Outline platelets.
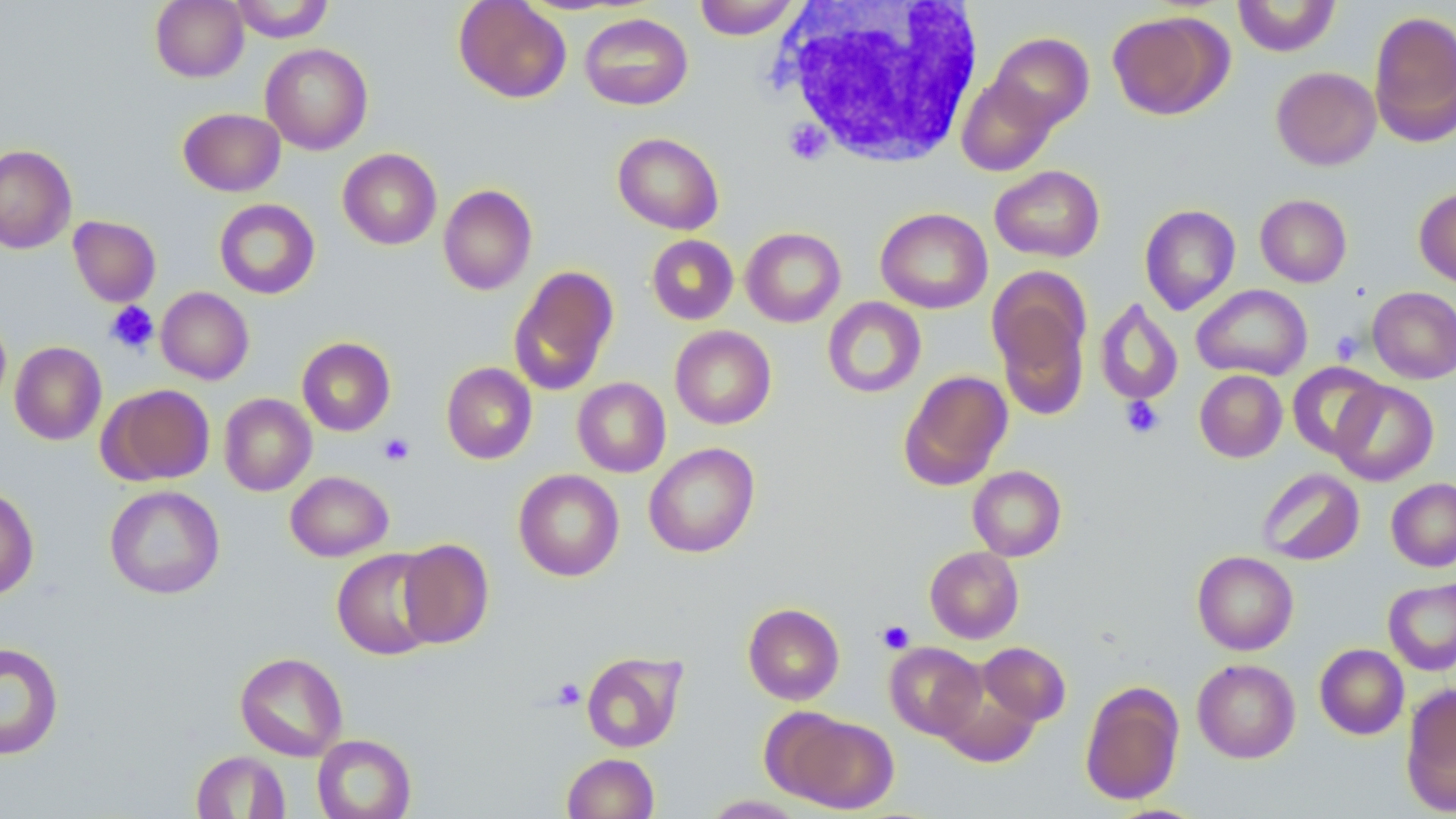
Approximate bounding boxes as (x1, y1, x2, y2) in pixels.
Platelets: (106, 301, 158, 354), (1330, 330, 1364, 364), (1121, 396, 1164, 439), (378, 433, 414, 466), (877, 620, 915, 654), (552, 679, 585, 709).

Uninfected red blood cell locations: (151, 0, 249, 82), (228, 0, 334, 42), (454, 0, 572, 103), (694, 0, 802, 40), (1232, 0, 1341, 57), (1106, 10, 1233, 120), (1368, 10, 1456, 147), (579, 12, 693, 110), (987, 32, 1094, 132), (260, 43, 373, 155), (1271, 66, 1381, 170), (957, 74, 1059, 176), (178, 108, 286, 196), (612, 132, 724, 235), (0, 144, 77, 254), (338, 148, 441, 250), (990, 165, 1105, 262), (438, 184, 537, 295), (1414, 187, 1456, 288), (1255, 194, 1352, 287), (214, 199, 320, 299), (1139, 204, 1241, 315), (875, 207, 992, 313), (68, 215, 161, 306), (741, 227, 846, 327), (646, 235, 738, 325), (508, 265, 619, 396), (989, 274, 1091, 420), (1192, 284, 1312, 380), (1367, 286, 1456, 384), (156, 287, 254, 384), (822, 297, 926, 398), (1095, 298, 1183, 406), (0, 312, 10, 412), (670, 325, 776, 429), (297, 336, 396, 436), (10, 341, 107, 445), (441, 362, 537, 464), (1287, 362, 1387, 459), (898, 369, 1013, 490), (1195, 369, 1287, 462), (572, 377, 671, 478), (1330, 380, 1438, 486), (98, 384, 215, 486), (219, 393, 316, 496), (644, 442, 760, 558), (968, 466, 1066, 561), (1256, 468, 1365, 566), (513, 469, 624, 581), (285, 471, 393, 561), (1386, 478, 1456, 571), (0, 485, 39, 600), (105, 485, 225, 599), (397, 539, 494, 648), (924, 546, 1024, 643), (332, 549, 440, 660), (1192, 551, 1298, 655), (1383, 577, 1456, 675), (743, 603, 845, 705), (0, 642, 64, 760), (885, 642, 986, 740), (978, 642, 1071, 725), (1315, 643, 1409, 739), (581, 651, 687, 753), (234, 652, 348, 761), (1192, 658, 1300, 763), (938, 679, 1041, 767), (1079, 681, 1185, 805), (1400, 684, 1456, 816), (775, 711, 899, 813), (312, 734, 416, 819), (191, 750, 290, 818), (562, 753, 659, 818), (702, 795, 806, 818). White blood cell locations: (771, 1, 987, 167). Slide-level diagnosis: no evidence of blood parasites. 1000x magnification. Light microscopy. Image is 1456×819 pixels. May-Grünwald-Giemsa-stained preparation. One field of a larger specimen. Thin blood film.